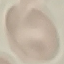

Summary:
  - Malaria status: uninfected
  - Capture: smartphone through the microscope eyepiece
  - Stain: Giemsa
  - Image type: cell patch, automatically extracted from a larger field of view and resized to 64 × 64 pixels
  - Preparation: thin blood smear